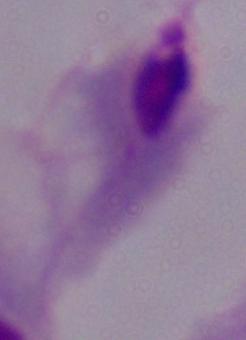
modality: micrograph
identification: trichomonad
magnification: 1000x